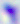

Summary:
  - Modality: photomicrograph
  - Magnification: 400x
  - Identification: Toxoplasma gondii